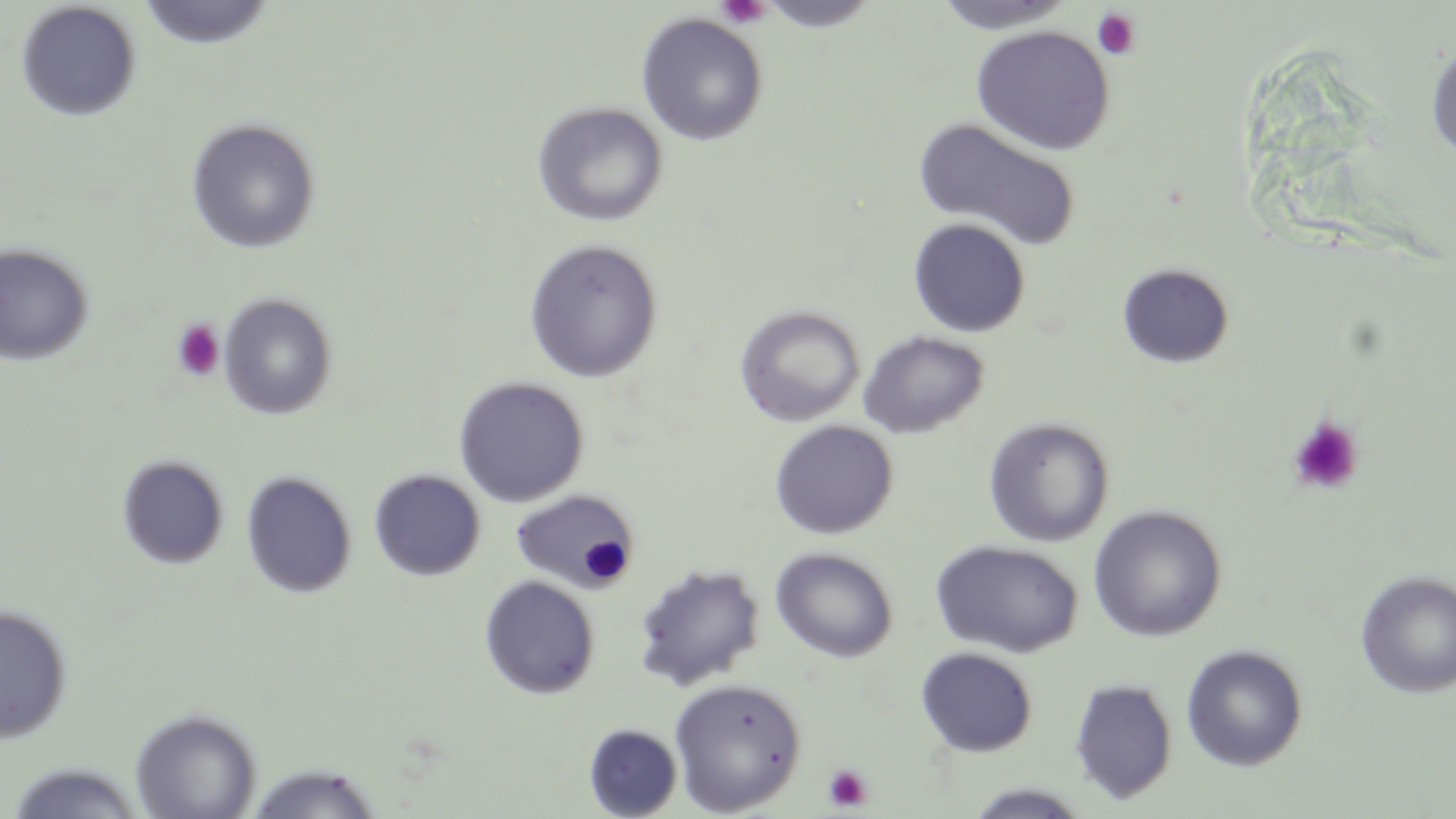 Approximate bounding boxes as [x1, y1, x2, y2] in pixels. Platelet locations: [716, 0, 772, 29], [1091, 8, 1141, 61], [171, 319, 226, 382], [1287, 416, 1364, 495], [823, 763, 872, 812]. Uninfected red blood cell locations: [930, 0, 1078, 33], [15, 1, 141, 121], [138, 1, 275, 49], [757, 1, 881, 32], [636, 12, 768, 146], [971, 25, 1116, 155], [1426, 34, 1456, 163], [532, 101, 668, 227], [913, 116, 1082, 253], [185, 117, 321, 254], [908, 217, 1031, 337], [522, 239, 664, 384], [0, 242, 95, 366], [1118, 263, 1234, 368], [218, 293, 338, 420], [734, 305, 865, 427], [858, 330, 990, 439], [453, 376, 590, 508], [983, 417, 1115, 548], [768, 420, 898, 539], [116, 454, 230, 570], [369, 469, 486, 581], [240, 471, 357, 598], [510, 488, 640, 592], [1088, 504, 1227, 641], [930, 539, 1084, 657], [769, 546, 899, 663], [632, 562, 765, 691], [1355, 571, 1456, 698], [479, 575, 601, 700], [0, 604, 72, 743], [1181, 644, 1308, 771], [915, 647, 1038, 757], [668, 677, 806, 815], [1069, 678, 1178, 804], [130, 706, 261, 818], [583, 723, 682, 817], [5, 761, 147, 818], [244, 762, 384, 818], [963, 783, 1091, 818]. Slide-level diagnosis: no evidence of blood parasites. 1000x magnification. Single field of view. Light microscopy. May-Grünwald-Giemsa-stained preparation. Image is 1456×819 pixels. Thin blood smear.